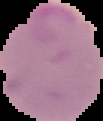
Summary:
  - Preparation: thin blood film
  - Image type: segmented cell region with the area outside set to black
  - Image size: 103×121 pixels
  - Result: Plasmodium parasites identified